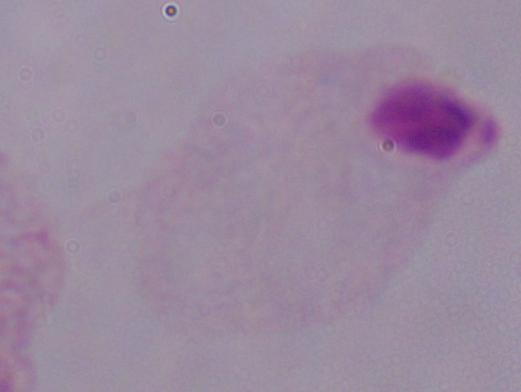

Photomicrograph. A trichomonad is seen. Captured at 1000x magnification.